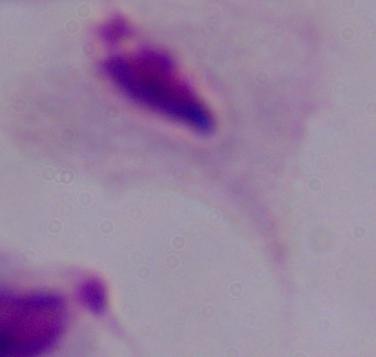

A trichomonad is shown. 1000x magnification. Photomicrograph.